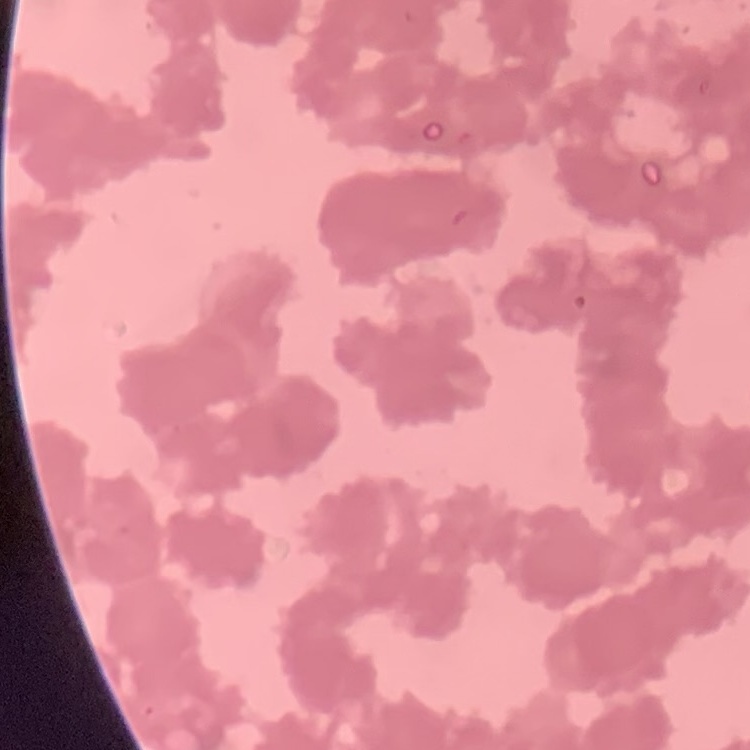

red blood cell morphology = rouleaux formation
image type = square crop of a larger photomicrograph
preparation = thin blood film
stain = Field's or Giemsa